Assess this cell for malaria.
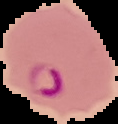

Parasitized.

Image is 118×124 pixels. Segmented cell region on a black background. From a thin blood smear.